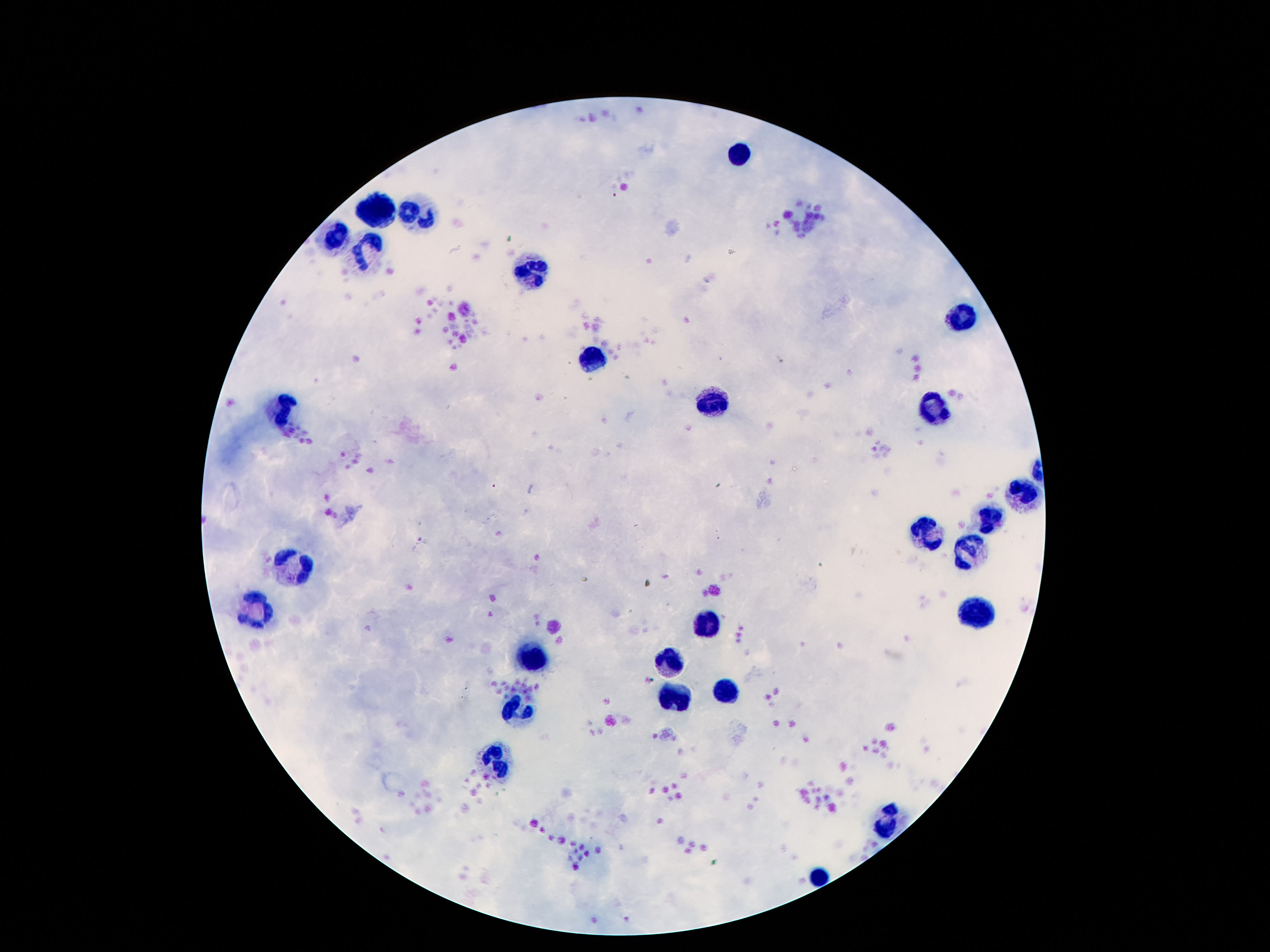
field_of_view: single
leukocyte_locations: 'approximate centers as (x, y) in pixels: (739, 155), (375, 211), (411, 213), (333, 239), (371, 255), (535, 270), (965, 316), (594, 360), (713, 402), (281, 407), (934, 414), (1022, 495), (993, 523), (928, 534), (967, 553), (293, 562), (258, 605), (978, 609), (709, 621), (671, 658), (533, 660), (726, 689), (676, 702), (518, 710), (499, 763), (884, 819), (818, 873)'
preparation: thick blood smear
image_size: 1270×952 pixels
magnification: 100x
stain: Giemsa
patient_malaria_status: negative
capture: smartphone camera through the microscope eyepiece